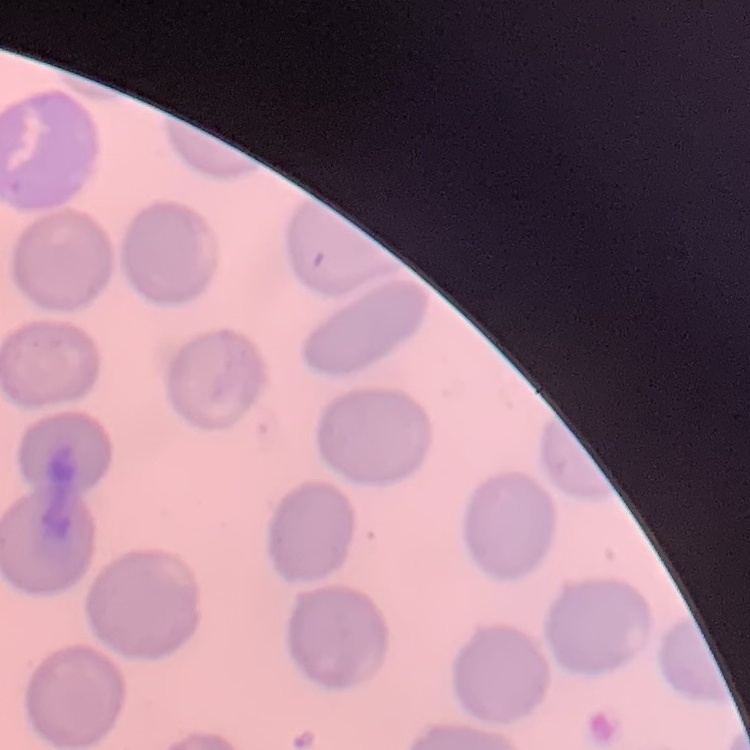

The red blood cells show no rouleaux formation. Thin blood film. Field's or Giemsa stain. One tile cut from a larger photomicrograph.